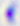

400x magnification. Micrograph. Toxoplasma gondii is seen.